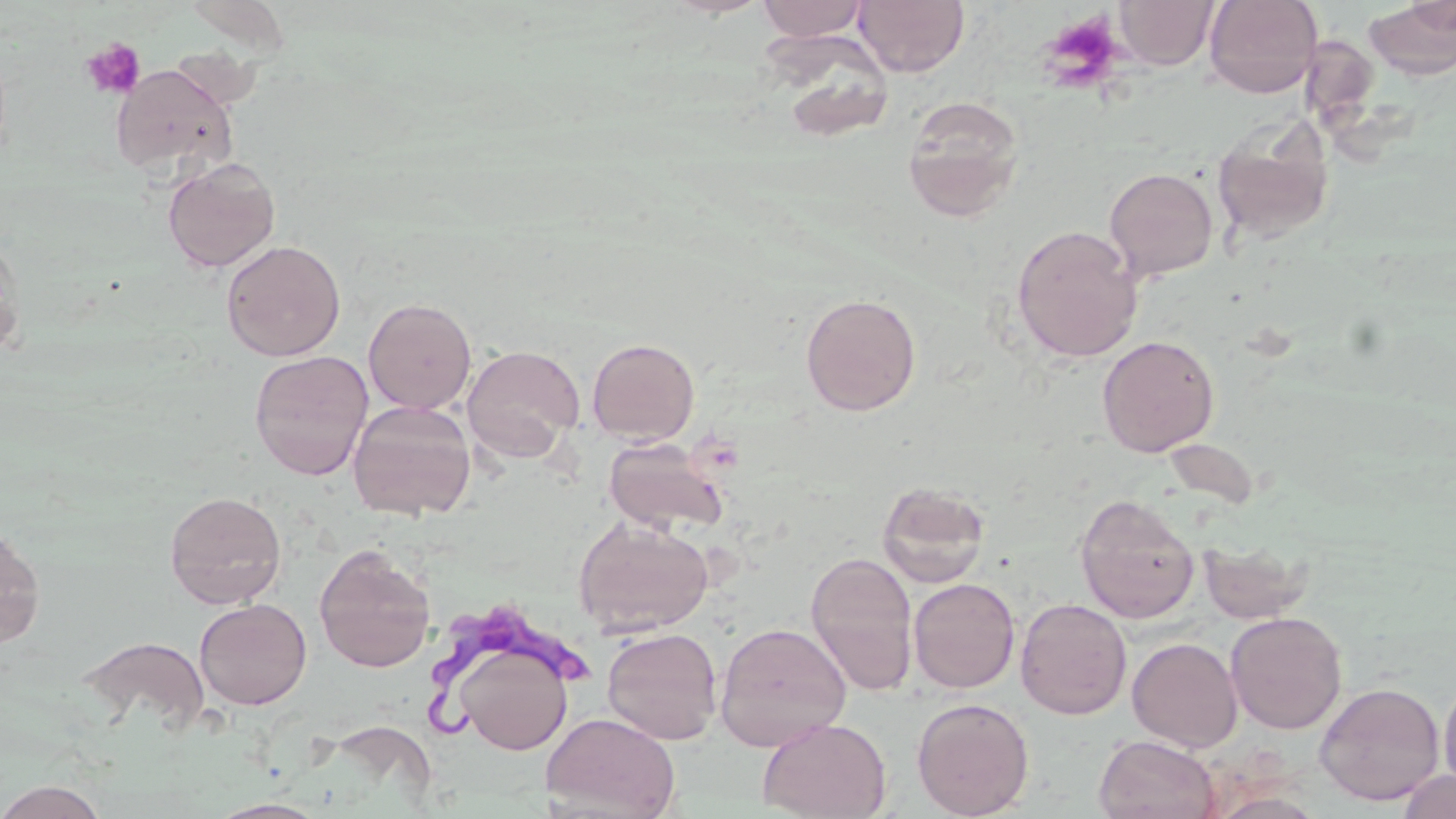
Trypanosoma brucei locations = approximate bounding boxes as (x1, y1, x2, y2) in pixels: (424, 608, 597, 741)
slide-level diagnosis = Trypanosoma brucei
platelet locations = approximate bounding boxes as (x1, y1, x2, y2) in pixels: (1036, 9, 1126, 93), (80, 37, 146, 100)
stain = May-Grünwald-Giemsa
image size = 1456×819 pixels
magnification = 1000x
field of view = one of a larger specimen
modality = light microscopy
preparation = thin blood smear
uninfected red blood cell locations = approximate bounding boxes as (x1, y1, x2, y2) in pixels: (755, 0, 870, 41), (853, 0, 969, 78), (1114, 0, 1219, 70), (1203, 0, 1323, 98), (1365, 4, 1456, 78), (761, 26, 898, 143), (1300, 34, 1380, 127), (112, 65, 238, 176), (903, 95, 1025, 221), (1212, 118, 1335, 245), (162, 157, 281, 273), (1104, 167, 1219, 281), (1011, 224, 1143, 363), (0, 231, 25, 359), (221, 239, 346, 361), (800, 293, 922, 416), (363, 297, 477, 414), (1097, 335, 1219, 457), (587, 337, 700, 445), (462, 344, 585, 461), (249, 350, 374, 481), (348, 400, 477, 521), (603, 437, 728, 536), (1164, 438, 1261, 510), (876, 482, 991, 588), (164, 490, 287, 610), (1075, 494, 1200, 623), (573, 516, 714, 637), (0, 521, 46, 648), (1198, 539, 1313, 624), (313, 543, 435, 674), (806, 551, 919, 695), (908, 577, 1020, 693), (1015, 597, 1132, 720), (194, 598, 312, 710), (1225, 612, 1347, 734), (714, 621, 852, 751), (601, 627, 723, 745), (78, 634, 210, 735), (1127, 636, 1244, 753), (453, 641, 576, 757), (1438, 670, 1456, 796), (1314, 681, 1445, 805), (911, 697, 1035, 818), (541, 711, 680, 818), (756, 716, 892, 819), (1094, 734, 1221, 819), (1395, 768, 1456, 819), (0, 779, 109, 819), (1204, 789, 1329, 818), (207, 798, 330, 818)